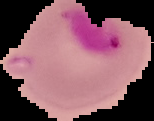 The area outside the segmented cell region is set to black. Image is 154×121 pixels. Result: malaria parasites detected. From a thin blood smear.